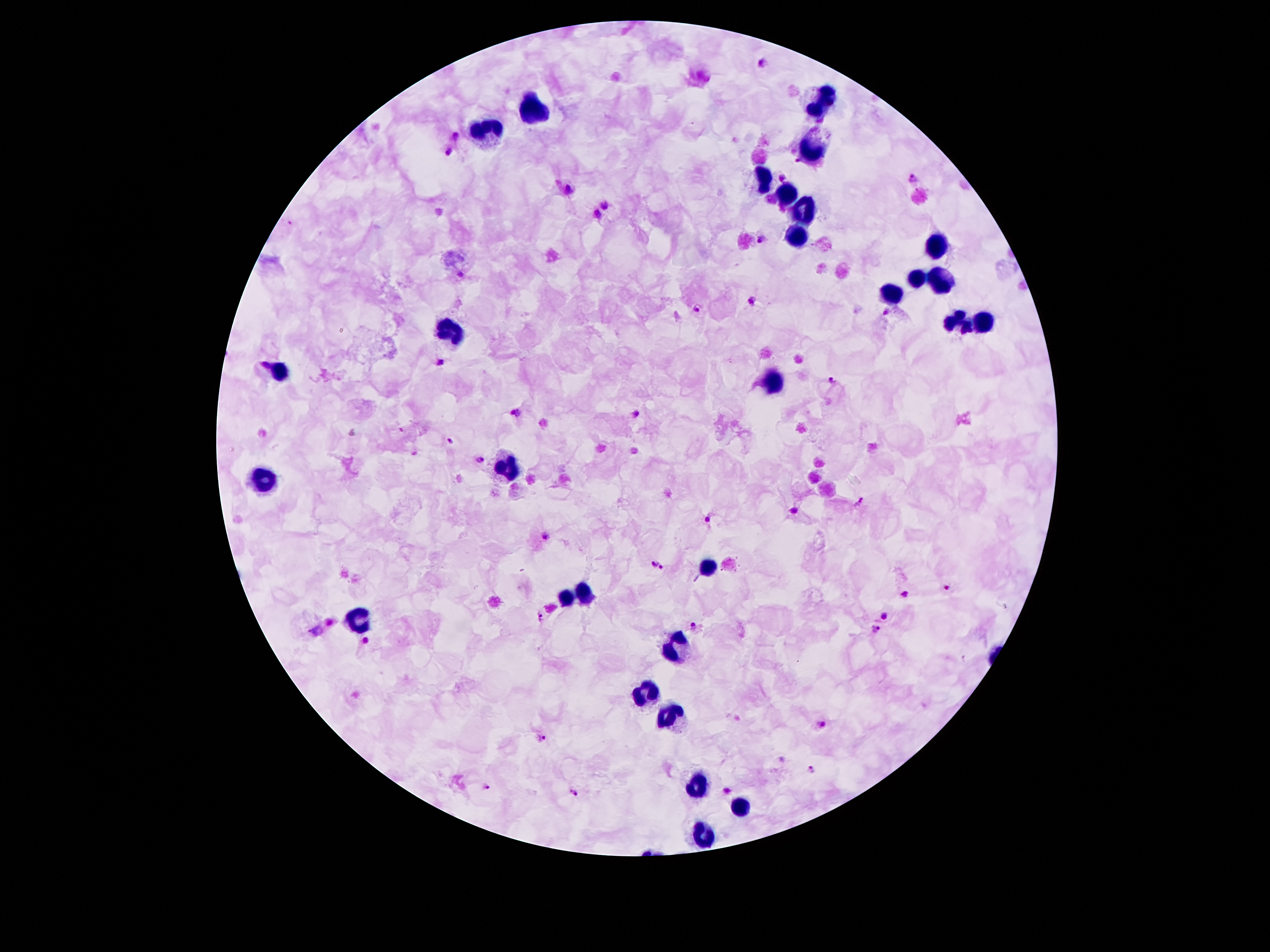

Approximate centers as [x, y] in pixels.
Summary:
  - Leukocyte locations: [821, 98], [532, 108], [490, 129], [815, 146], [765, 182], [788, 195], [805, 209], [792, 235], [935, 249], [914, 277], [939, 281], [887, 291], [958, 321], [985, 323], [454, 327], [278, 371], [775, 382], [502, 470], [265, 478], [708, 568], [565, 592], [588, 592], [358, 619], [683, 644], [645, 692], [670, 718], [696, 783], [737, 808], [702, 835]
  - Plasmodium parasite locations: [761, 65], [456, 135], [448, 150], [799, 161], [782, 176], [913, 180], [570, 189], [604, 206], [597, 215], [763, 237], [752, 301], [696, 308], [883, 313], [441, 361], [264, 364], [830, 379], [518, 412], [635, 414], [450, 441], [482, 457], [860, 502], [795, 511], [708, 519], [546, 537], [653, 565], [662, 568], [947, 588], [905, 595], [541, 616], [884, 617], [693, 625], [874, 629], [315, 631], [824, 723], [543, 738], [812, 770], [487, 787], [727, 790], [575, 792]
  - Patient malaria status: positive for Plasmodium falciparum
  - Image size: 1270×952 pixels
  - Preparation: thick blood film
  - Magnification: 100x
  - Stain: Giemsa
  - Capture: smartphone through the microscope eyepiece
  - Field of view: single